Give the position of every malaria parasite.
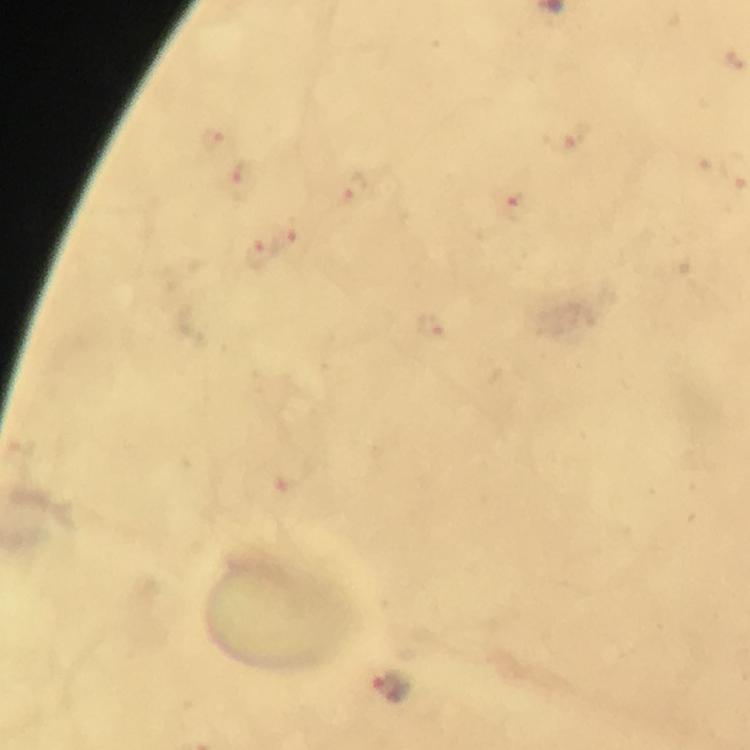
Approximate centers as {x, y} in pixels.
Malaria parasites: {391, 687}.

Summary:
  - Image size: 750×750 pixels
  - Magnification: 100x
  - Stain: Giemsa
  - Preparation: thick blood smear
  - Cropped from: one field of view
  - Capture: smartphone mounted on the microscope
  - Immersion oil: applied
  - Context: from a malaria diagnostic workup